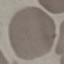
Summary:
  - Malaria status: uninfected
  - Image type: automatically extracted cell patch, resized to 64 × 64 pixels
  - Preparation: thin blood smear
  - Stain: Giemsa
  - Capture: smartphone through the microscope eyepiece